Look for Plasmodium parasites.
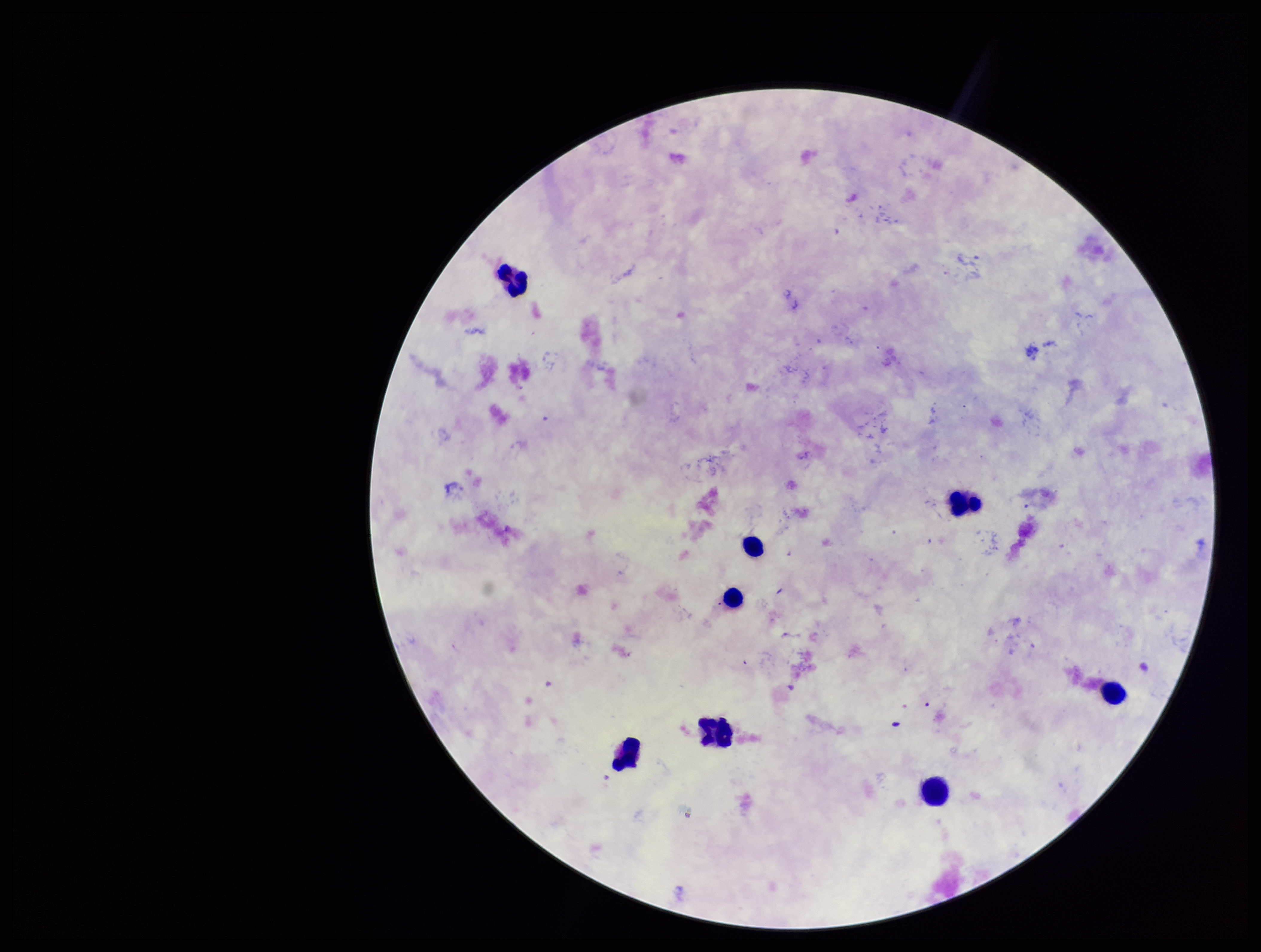

None identified.

Summary:
  - Preparation: thick
  - Parasite count: 0
  - Patient malaria status: negative
  - Stain: Giemsa
  - Image size: 1261×952 pixels
  - Leukocyte count: 8
  - Capture: smartphone photograph through the microscope eyepiece
  - Field of view: single